Classify this cell by malaria status.
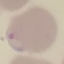

It is parasitized.

{
  "image_type": "cell patch, automatically extracted from a larger field of view and resized to 64 × 64 pixels",
  "stain": "Giemsa",
  "capture": "smartphone camera at the microscope eyepiece",
  "preparation": "thin smear"
}